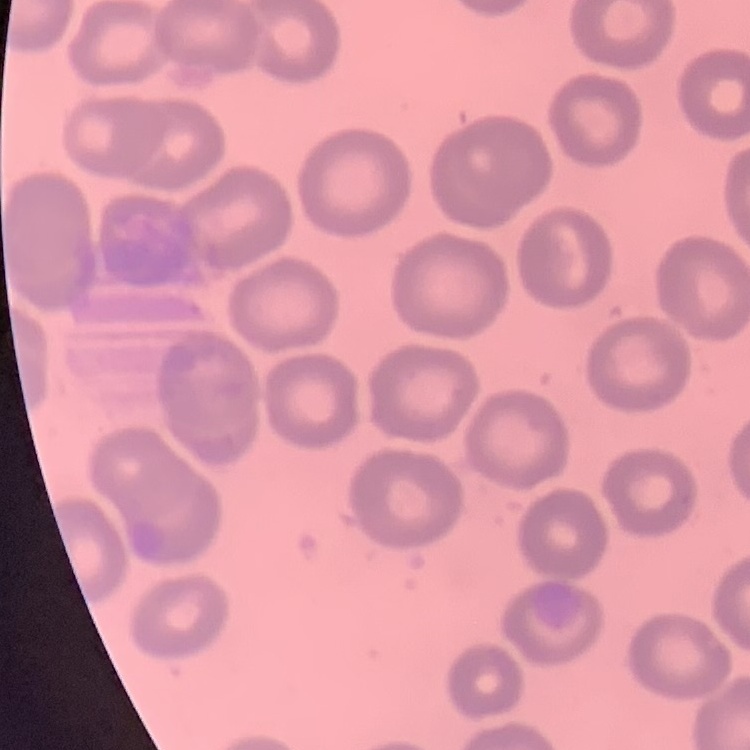

The erythrocytes show no rouleaux formation. Stained with either Field's or Giemsa. Square crop of a larger photomicrograph. Thin peripheral smear.